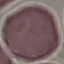

Summary:
  - Result: no malaria parasites detected
  - Stain: Giemsa
  - Capture: smartphone through the microscope eyepiece
  - Image type: cell patch, automatically extracted from a larger field of view and resized to 64 × 64 pixels
  - Preparation: thin blood film